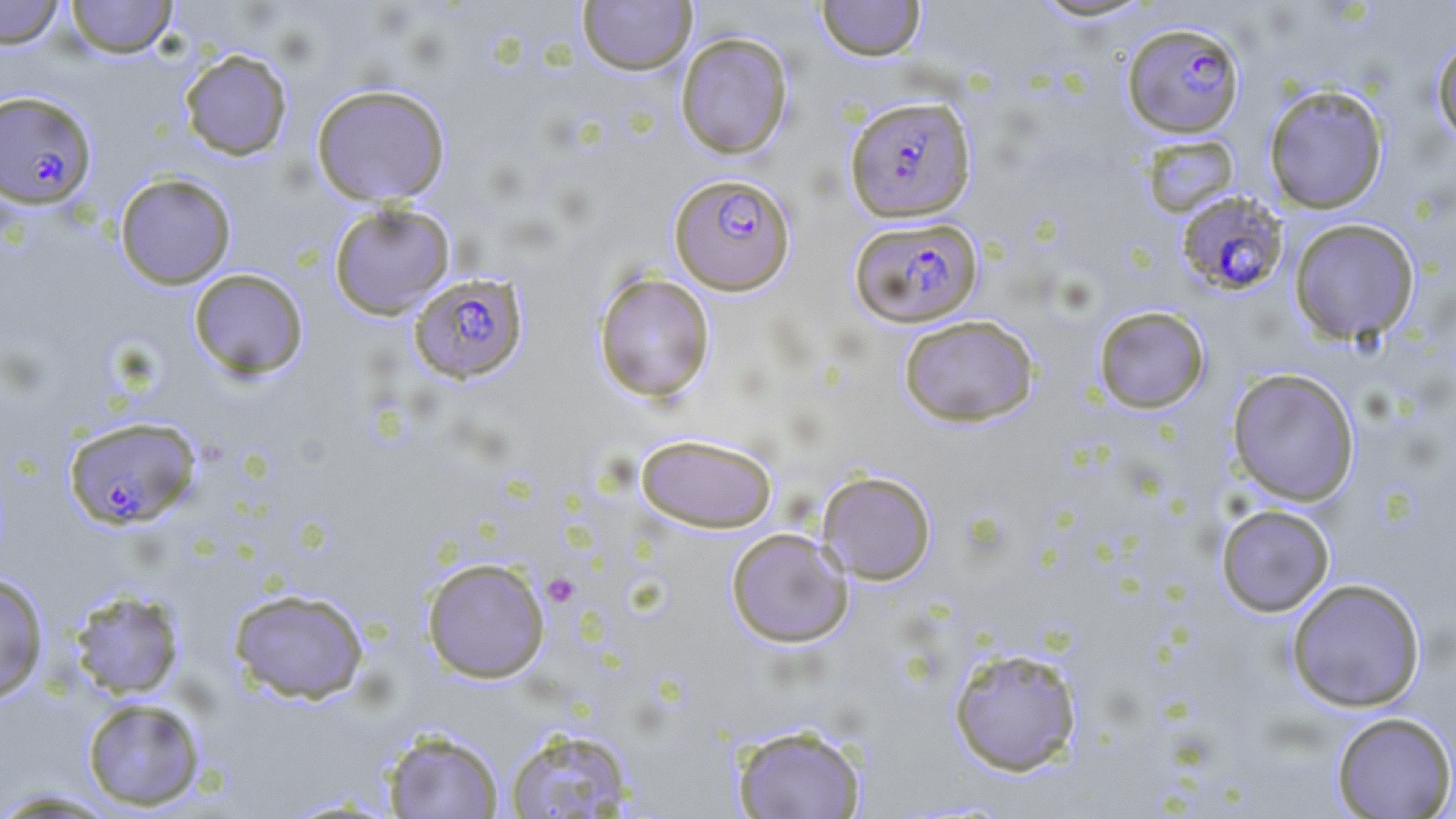

{
  "slide_level_diagnosis": "Plasmodium falciparum",
  "field_of_view": "single",
  "uninfected_red_blood_cell_locations": "approximate bounding boxes as [x1, y1, x2, y2] in pixels: [0, 0, 66, 49], [65, 0, 178, 58], [816, 0, 926, 61], [1026, 0, 1161, 23], [577, 1, 697, 75], [674, 32, 793, 159], [1431, 35, 1456, 149], [178, 49, 293, 161], [310, 83, 451, 207], [1263, 84, 1389, 214], [1142, 136, 1242, 219], [114, 173, 237, 289], [328, 202, 456, 319], [1288, 217, 1420, 346], [188, 268, 309, 380], [593, 272, 716, 403], [1093, 305, 1210, 413], [898, 314, 1039, 427], [1227, 368, 1360, 505], [635, 432, 778, 533], [817, 470, 937, 585], [1216, 504, 1335, 617], [725, 528, 853, 648], [421, 556, 550, 683], [0, 573, 49, 704], [1286, 577, 1426, 712], [67, 587, 186, 700], [228, 587, 369, 704], [948, 646, 1083, 776], [80, 697, 207, 811], [1331, 711, 1456, 818], [731, 723, 868, 819], [504, 725, 637, 818], [381, 728, 504, 818], [0, 787, 123, 817]",
  "magnification": "1000x",
  "plasmodium_falciparum_infected_red_blood_cell_locations": "approximate bounding boxes as [x1, y1, x2, y2] in pixels: [1122, 21, 1245, 138], [0, 90, 98, 210], [844, 95, 976, 222], [669, 172, 796, 295], [1176, 191, 1291, 296], [850, 217, 982, 328], [408, 273, 529, 384], [63, 415, 201, 531]",
  "modality": "optical microscopy",
  "platelet_locations": "approximate bounding boxes as [x1, y1, x2, y2] in pixels: [542, 573, 580, 607]",
  "preparation": "thin blood film",
  "stain": "May-Grünwald-Giemsa",
  "image_size": "1456×819 pixels"
}